Classify this cell by malaria status.
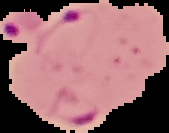
Parasitized.

Segmented cell region on a black background. Image is 169×133 pixels. From a thin blood film.